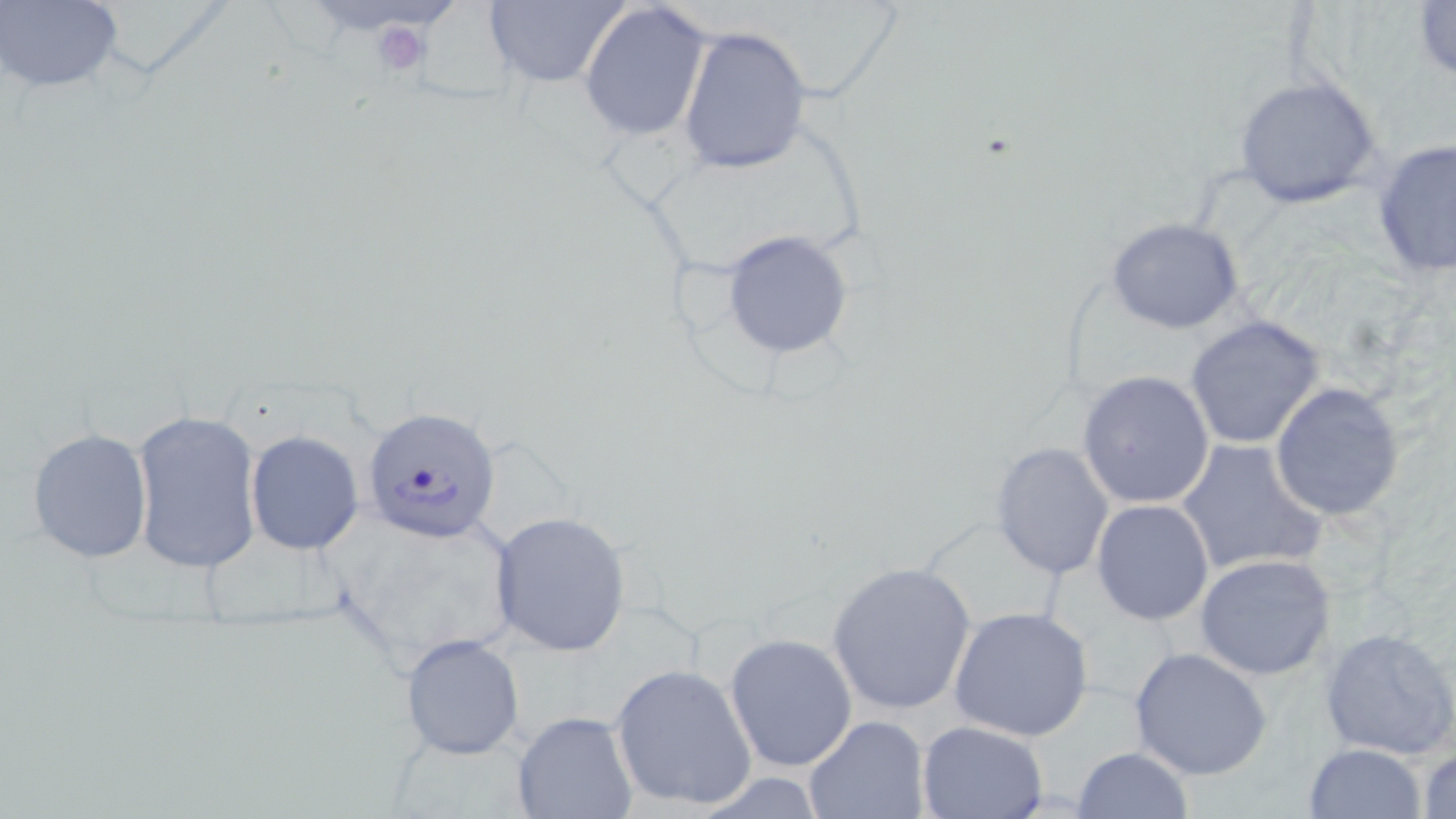
Summary:
  - Coordinate format: approximate bounding boxes as named x1/y1/x2/y2 corners in pixels
  - Uninfected red blood cell locations: (x1=1, y1=0, x2=122, y2=93), (x1=482, y1=0, x2=630, y2=89), (x1=1411, y1=0, x2=1456, y2=79), (x1=579, y1=2, x2=712, y2=141), (x1=677, y1=25, x2=812, y2=175), (x1=1234, y1=75, x2=1385, y2=211), (x1=1371, y1=137, x2=1456, y2=280), (x1=1106, y1=217, x2=1245, y2=335), (x1=720, y1=231, x2=856, y2=359), (x1=1185, y1=315, x2=1328, y2=450), (x1=1077, y1=369, x2=1218, y2=509), (x1=1268, y1=383, x2=1404, y2=521), (x1=129, y1=408, x2=263, y2=574), (x1=27, y1=427, x2=154, y2=564), (x1=244, y1=430, x2=364, y2=555), (x1=1174, y1=438, x2=1326, y2=578), (x1=990, y1=440, x2=1115, y2=581), (x1=1091, y1=498, x2=1214, y2=625), (x1=328, y1=507, x2=524, y2=669), (x1=490, y1=511, x2=633, y2=656), (x1=1195, y1=553, x2=1336, y2=680), (x1=826, y1=561, x2=976, y2=715), (x1=948, y1=605, x2=1097, y2=743), (x1=1318, y1=626, x2=1456, y2=761), (x1=401, y1=632, x2=525, y2=760), (x1=723, y1=632, x2=859, y2=773), (x1=1129, y1=645, x2=1275, y2=781), (x1=609, y1=664, x2=758, y2=812), (x1=511, y1=712, x2=638, y2=818), (x1=803, y1=714, x2=930, y2=819), (x1=916, y1=719, x2=1050, y2=819), (x1=1304, y1=743, x2=1426, y2=819), (x1=1416, y1=743, x2=1456, y2=819), (x1=1071, y1=745, x2=1197, y2=818)
  - Platelet locations: (x1=367, y1=18, x2=432, y2=78)
  - Plasmodium falciparum-infected red blood cell locations: (x1=359, y1=408, x2=501, y2=543)
  - Slide-level diagnosis: Plasmodium falciparum
  - Image size: 1456×819 pixels
  - Magnification: 1000x
  - Field of view: one of a larger specimen
  - Modality: light microscopy
  - Stain: May-Grünwald-Giemsa
  - Preparation: thin blood film